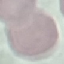

{
  "result": "no malaria parasites detected",
  "preparation": "thin smear",
  "image_type": "automatically extracted cell patch, resized to 64 × 64 pixels",
  "capture": "smartphone camera at the microscope eyepiece",
  "stain": "Giemsa"
}